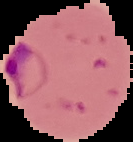

From a thin blood smear. Malaria status: parasitized. Image is 133×142 pixels. The area outside the segmented cell region is set to black.